Assess this cell for malaria.
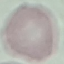
It is uninfected.

Summary:
  - Image type: cell patch, automatically extracted from a larger field of view and resized to 64 × 64 pixels
  - Capture: smartphone camera at the microscope eyepiece
  - Stain: Giemsa
  - Preparation: thin blood film